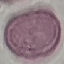
Summary:
  - Malaria status: uninfected
  - Preparation: thin blood film
  - Stain: Giemsa
  - Image type: cell patch, automatically extracted from a larger field of view and resized to 64 × 64 pixels
  - Capture: smartphone camera at the microscope eyepiece